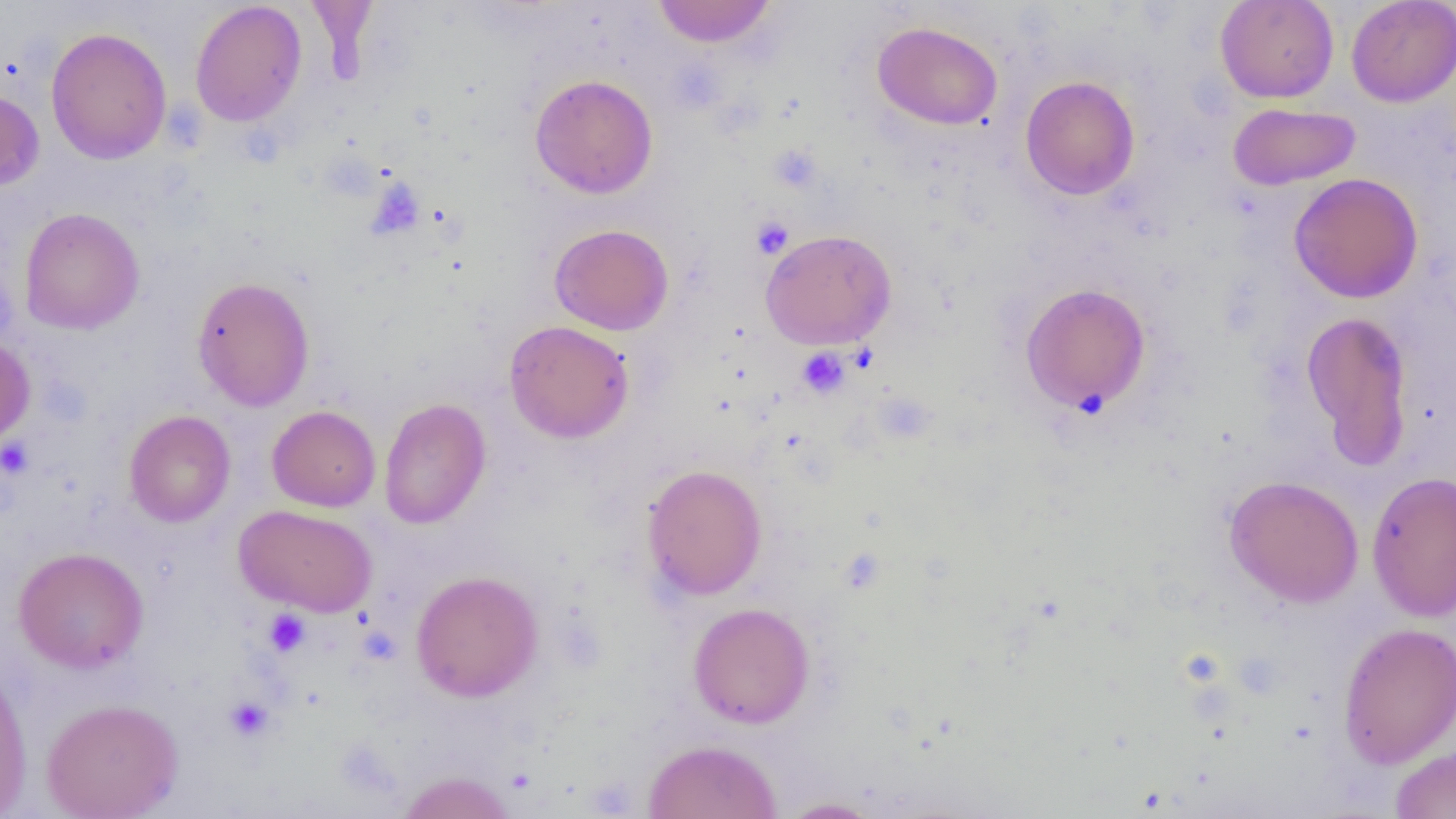

Summary:
  - Coordinate format: approximate bounding boxes as [x1, y1, x2, y2] in pixels
  - Platelet locations: [368, 178, 425, 239], [751, 216, 794, 259], [796, 347, 851, 399], [1, 437, 34, 479], [263, 609, 311, 657], [223, 696, 275, 742]
  - Uninfected red blood cell locations: [305, 0, 380, 79], [651, 0, 777, 48], [1215, 0, 1339, 103], [1346, 0, 1456, 107], [190, 1, 307, 127], [873, 21, 1003, 130], [45, 26, 172, 164], [530, 74, 658, 199], [1020, 75, 1140, 200], [0, 88, 44, 191], [1227, 102, 1362, 190], [1288, 173, 1423, 303], [19, 207, 145, 334], [549, 223, 674, 335], [760, 228, 897, 350], [191, 276, 315, 411], [1020, 282, 1152, 414], [1300, 309, 1414, 471], [503, 320, 634, 443], [0, 336, 35, 445], [379, 398, 491, 529], [267, 405, 381, 512], [124, 410, 236, 527], [642, 463, 767, 601], [1366, 471, 1456, 621], [1223, 475, 1364, 608], [234, 504, 377, 617], [13, 546, 149, 673], [410, 570, 543, 702], [687, 602, 815, 728], [1337, 621, 1456, 768], [0, 662, 33, 817], [41, 697, 184, 819], [642, 739, 783, 819], [1389, 745, 1456, 818], [395, 771, 517, 818], [776, 797, 885, 818]
  - Slide-level diagnosis: negative for blood parasites
  - Magnification: 1000x
  - Field of view: one of a larger specimen
  - Image size: 1456×819 pixels
  - Modality: optical microscopy
  - Preparation: thin blood film